Locate and identify every blood parasite.
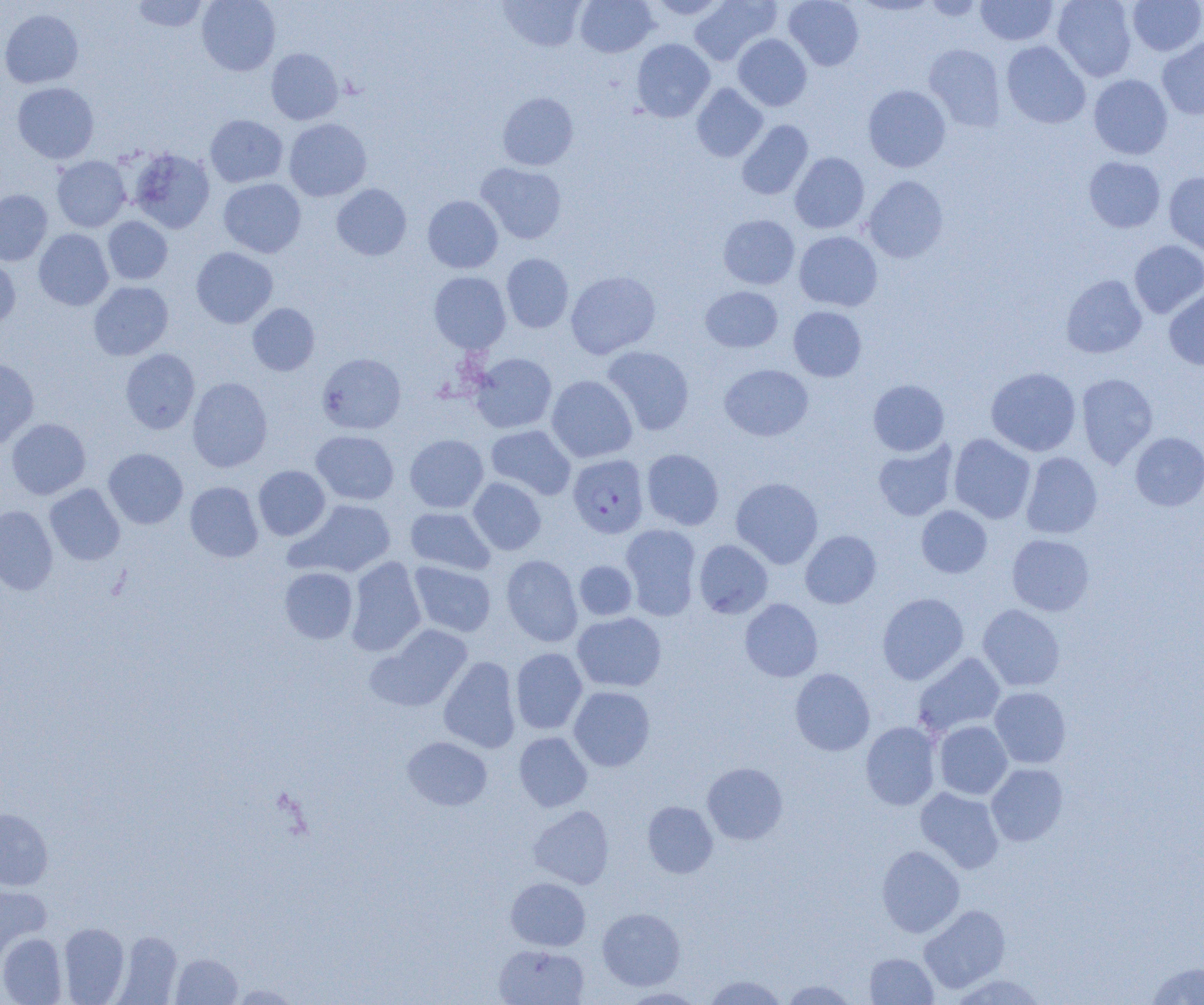
Approximate bounding boxes as [x1, y1, x2, y2] in pixels.
Plasmodium falciparum-infected red blood cells: [568, 454, 649, 538].
No Plasmodium ovale, Plasmodium malariae, Plasmodium vivax, Babesia divergens, or Trypanosoma brucei observed.

slide_level_diagnosis: Plasmodium falciparum
magnification: 1000x
field_of_view: one of a larger specimen
modality: optical microscopy
uninfected_red_blood_cell_locations: 'approximate bounding boxes as [x1, y1, x2, y2] in pixels: [130, 0, 209, 32], [197, 0, 281, 76], [499, 0, 586, 52], [574, 0, 658, 57], [647, 0, 729, 19], [689, 0, 780, 65], [784, 0, 864, 70], [853, 0, 938, 16], [921, 0, 987, 22], [976, 0, 1058, 45], [1052, 0, 1137, 82], [1127, 0, 1204, 56], [0, 8, 84, 89], [733, 34, 812, 111], [1157, 37, 1204, 120], [631, 38, 714, 122], [1001, 41, 1090, 128], [923, 44, 1006, 131], [266, 48, 344, 125], [1088, 74, 1173, 159], [11, 82, 100, 164], [691, 84, 768, 162], [863, 85, 951, 172], [497, 92, 579, 171], [205, 114, 288, 187], [284, 118, 372, 201], [736, 120, 813, 200], [127, 148, 215, 234], [790, 152, 870, 234], [51, 156, 131, 232], [1083, 156, 1165, 233], [475, 162, 567, 244], [1164, 171, 1204, 256], [862, 175, 948, 263], [218, 178, 306, 258], [331, 183, 411, 260], [0, 189, 53, 266], [423, 195, 503, 273], [718, 214, 800, 289], [102, 216, 173, 285], [34, 228, 114, 310], [794, 231, 883, 311], [1129, 240, 1204, 318], [191, 247, 278, 328], [501, 253, 574, 332], [0, 255, 21, 332], [566, 270, 661, 359], [429, 272, 510, 353], [1061, 274, 1147, 358], [88, 281, 174, 360], [700, 286, 783, 352], [1164, 287, 1204, 370], [247, 303, 320, 376], [788, 306, 867, 381], [602, 346, 695, 435], [120, 348, 200, 434], [317, 352, 406, 434], [470, 353, 557, 433], [0, 358, 39, 448], [719, 364, 813, 441], [986, 367, 1081, 456], [1076, 373, 1159, 468], [547, 375, 637, 462], [187, 377, 273, 472], [868, 379, 950, 456], [6, 418, 91, 499], [485, 425, 575, 499], [311, 430, 399, 505], [1130, 432, 1204, 511], [949, 433, 1036, 523], [405, 434, 488, 513], [873, 440, 958, 521], [103, 448, 188, 529], [642, 449, 724, 530], [1021, 451, 1103, 539], [253, 465, 330, 540], [468, 477, 546, 555], [731, 477, 823, 568], [185, 481, 263, 562], [45, 483, 125, 565], [289, 499, 396, 577], [916, 505, 992, 578], [0, 506, 58, 595], [405, 507, 495, 575], [620, 524, 701, 620], [800, 530, 881, 608], [1007, 534, 1095, 616], [694, 539, 773, 618], [501, 555, 583, 647], [345, 557, 426, 656], [574, 560, 637, 620], [409, 562, 496, 637], [279, 567, 358, 643], [877, 592, 969, 685], [739, 598, 823, 682], [977, 604, 1065, 692], [572, 612, 666, 692], [365, 624, 473, 712], [511, 648, 588, 734], [912, 651, 1006, 738], [439, 656, 521, 753], [790, 668, 875, 756], [568, 686, 655, 772], [990, 686, 1071, 768], [933, 720, 1013, 800], [861, 721, 941, 810], [514, 731, 592, 811], [402, 736, 492, 810], [702, 762, 787, 844], [986, 763, 1068, 846], [915, 787, 1005, 873], [642, 800, 718, 877], [529, 806, 614, 888], [0, 808, 53, 890], [876, 845, 965, 937], [506, 877, 590, 951], [0, 885, 52, 962], [919, 904, 1011, 993], [597, 907, 685, 990], [59, 922, 129, 1004], [113, 931, 183, 1004], [0, 932, 67, 1004], [493, 944, 589, 1004], [864, 952, 938, 1004], [172, 953, 243, 1004], [1144, 961, 1204, 1004], [950, 973, 1051, 1005], [702, 974, 789, 1005], [780, 979, 859, 1005], [228, 983, 301, 1004], [619, 987, 706, 1004]'
preparation: thin blood film
image_size: 1204×1005 pixels